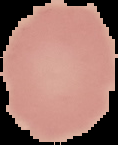
Cell region segmented out of the field of view; the surrounding area is masked to black. Image is 118×145 pixels. Malaria status: uninfected. From a thin blood smear.